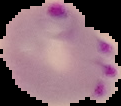

Summary:
  - Image size: 121×106 pixels
  - Preparation: thin blood smear
  - Malaria status: parasitized
  - Image type: segmented cell region on a black background